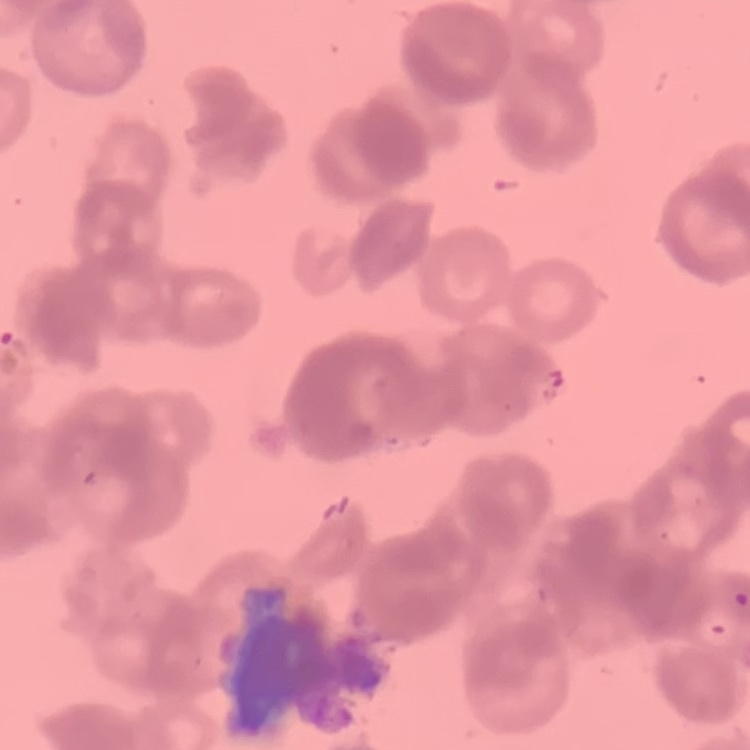 The red blood cells exhibit rouleaux formation. Thin blood film. Field's or Giemsa stain. Square crop of a larger photomicrograph.